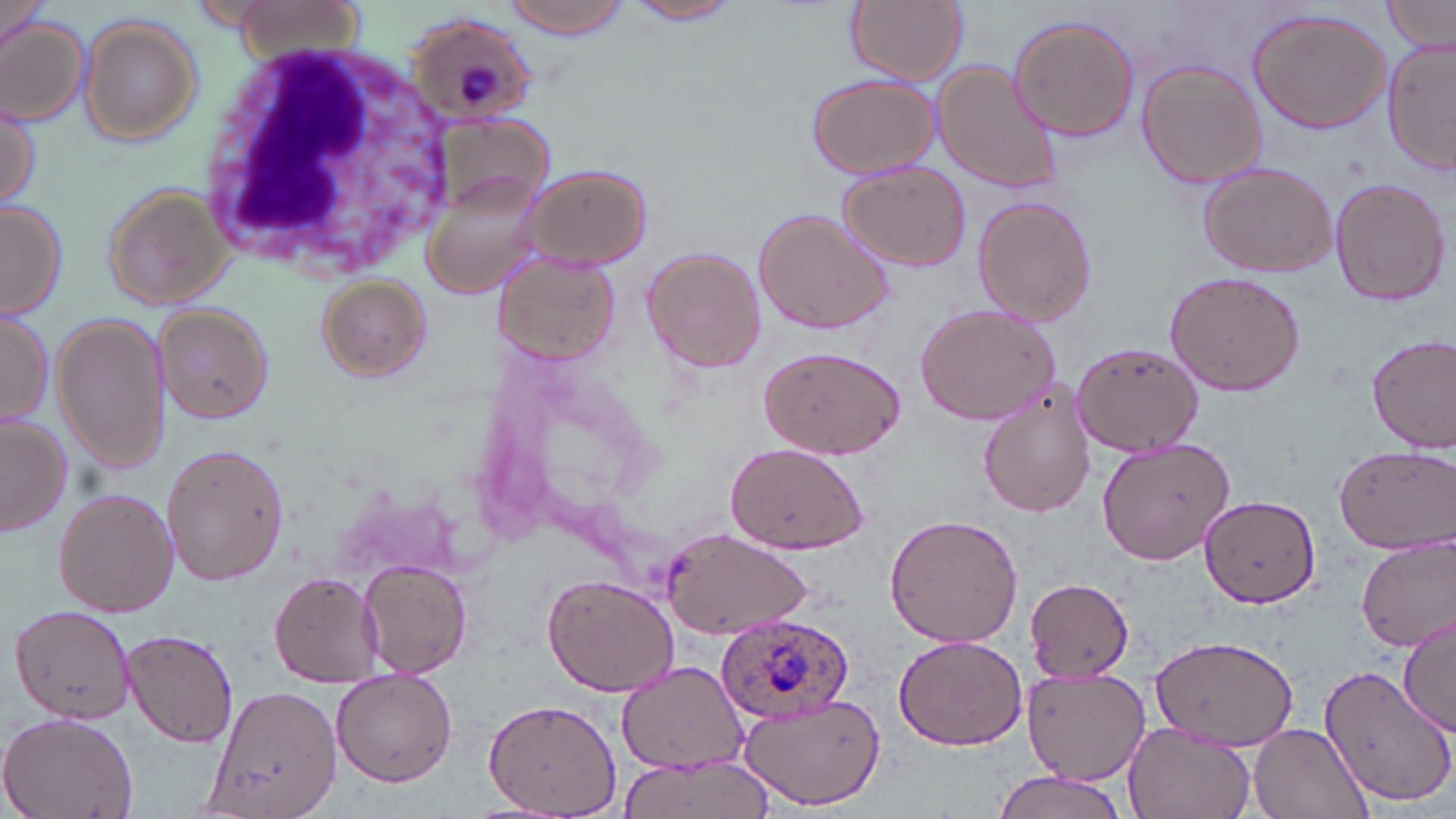

Summary:
  - Coordinate format: approximate bounding boxes as (x1, y1, x2, y2) in pixels
  - Plasmodium ovale-infected red blood cell locations: (406, 13, 541, 126), (718, 614, 857, 724)
  - White blood cell locations: (198, 41, 458, 283)
  - Uninfected red blood cell locations: (501, 0, 634, 41), (845, 0, 968, 86), (1383, 0, 1453, 56), (625, 1, 746, 25), (1247, 6, 1391, 135), (0, 11, 91, 126), (1008, 14, 1140, 142), (78, 16, 203, 144), (1382, 37, 1455, 177), (929, 59, 1065, 193), (1135, 59, 1269, 190), (806, 74, 939, 180), (0, 96, 41, 215), (838, 161, 971, 273), (1195, 161, 1339, 278), (516, 162, 652, 271), (418, 165, 559, 305), (1328, 177, 1450, 307), (101, 180, 232, 311), (972, 194, 1098, 325), (0, 200, 68, 319), (752, 206, 894, 337), (641, 247, 766, 372), (494, 256, 621, 365), (1160, 271, 1306, 396), (314, 274, 431, 380), (914, 301, 1063, 426), (0, 306, 55, 426), (152, 306, 272, 423), (53, 313, 171, 475), (1366, 332, 1456, 454), (1070, 341, 1204, 458), (756, 345, 906, 460), (978, 389, 1098, 517), (0, 414, 72, 536), (1096, 434, 1237, 565), (160, 442, 291, 588), (724, 442, 871, 555), (1332, 443, 1454, 554), (53, 488, 181, 617), (1200, 496, 1320, 606), (883, 512, 1025, 650), (656, 527, 812, 639), (1357, 535, 1455, 651), (357, 560, 473, 678), (541, 572, 680, 696), (270, 573, 382, 687), (1025, 580, 1133, 681), (5, 606, 139, 721), (1397, 615, 1456, 736), (120, 628, 241, 750), (892, 634, 1029, 750), (1151, 634, 1301, 751), (616, 661, 751, 774), (1317, 662, 1456, 809), (1022, 667, 1147, 785), (330, 670, 459, 787), (201, 686, 349, 819), (735, 690, 885, 810), (485, 700, 622, 817), (0, 711, 137, 819), (1122, 721, 1255, 819), (1249, 724, 1373, 819), (613, 755, 773, 819), (992, 772, 1134, 819)
  - Slide-level diagnosis: Plasmodium ovale
  - Field of view: single
  - Image size: 1456×819 pixels
  - Preparation: thin blood smear
  - Stain: May-Grünwald-Giemsa
  - Modality: optical microscopy
  - Magnification: 1000x